State which parasite is depicted.
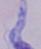

This is a trypanosome.

Summary:
  - Magnification: 1000x
  - Modality: photomicrograph